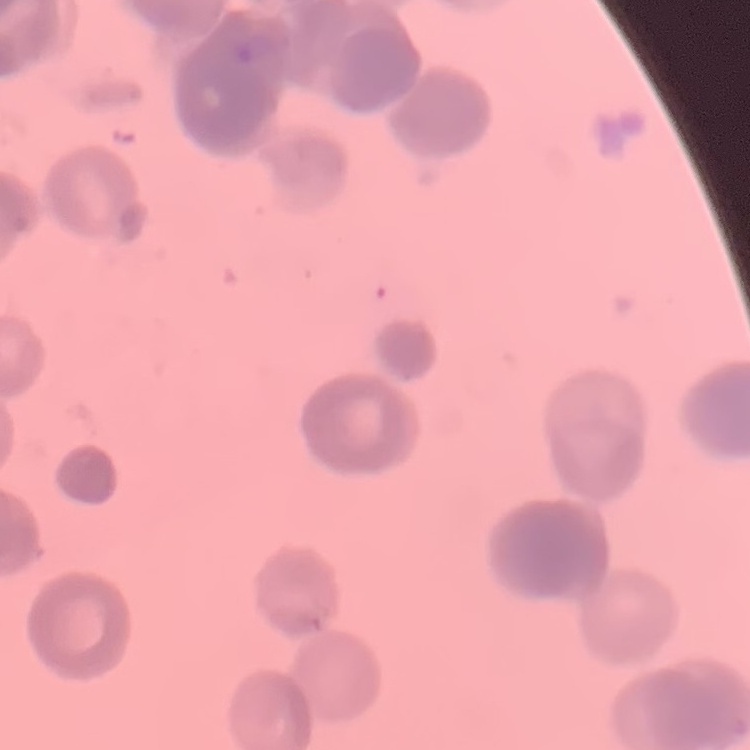

red blood cell morphology = rouleaux formation
preparation = thin blood film
stain = Field's or Giemsa
image type = one tile cut from a larger photomicrograph